Name the parasite shown.
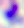
Toxoplasma gondii.

Summary:
  - Magnification: 400x
  - Modality: photomicrograph